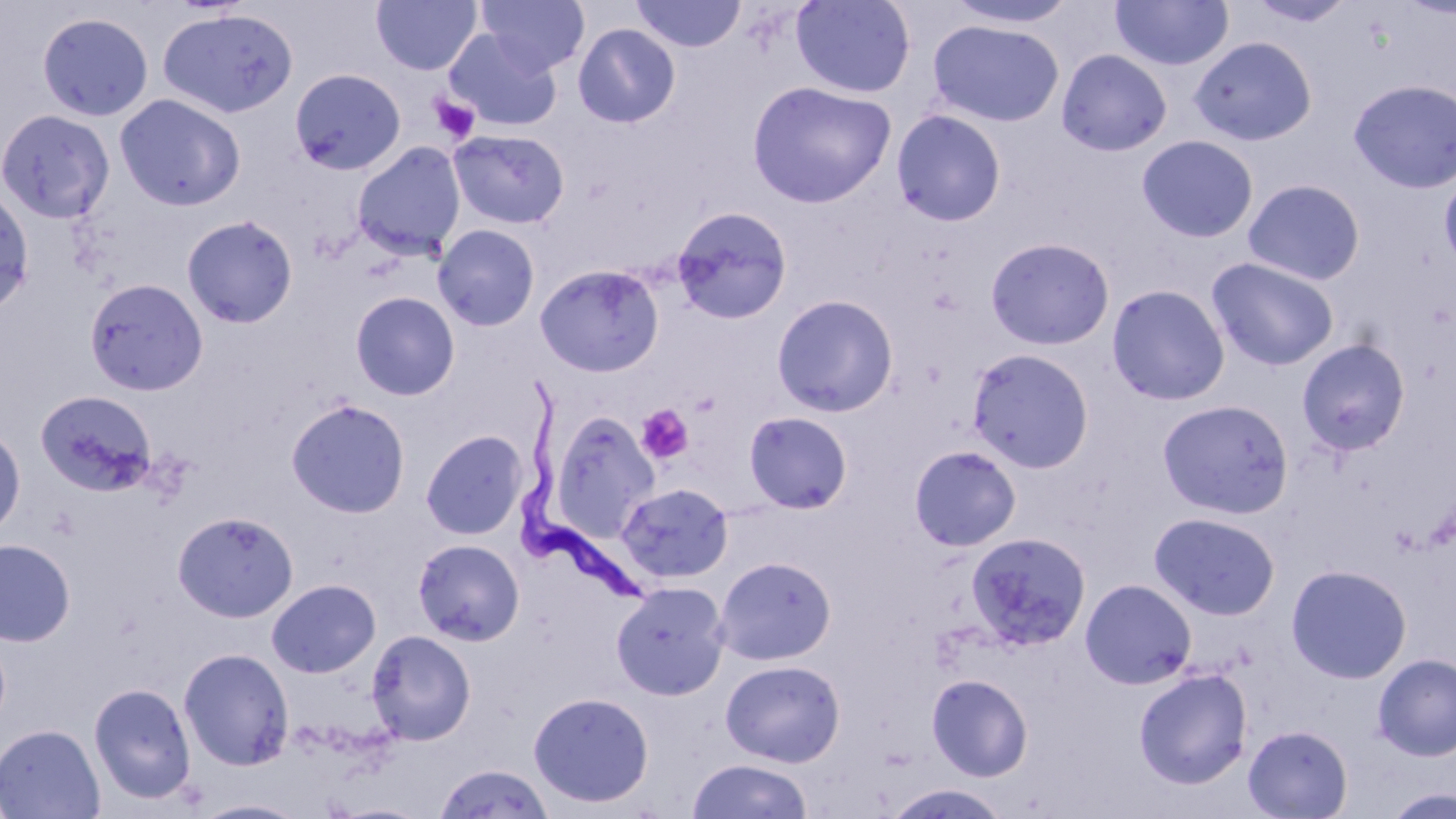
Trypanosoma brucei locations = approximate bounding boxes as (x1, y1, x2, y2) in pixels: (515, 377, 661, 608)
slide-level diagnosis = Trypanosoma brucei
magnification = 1000x
preparation = thin blood smear
stain = May-Grünwald-Giemsa
uninfected red blood cell locations = approximate bounding boxes as (x1, y1, x2, y2) in pixels: (371, 0, 481, 75), (476, 0, 589, 76), (630, 0, 746, 52), (790, 0, 916, 98), (941, 0, 1079, 30), (1110, 0, 1234, 72), (1245, 1, 1357, 28), (157, 8, 299, 119), (36, 11, 154, 122), (928, 20, 1065, 127), (573, 23, 681, 128), (444, 29, 562, 132), (1188, 36, 1318, 146), (1057, 49, 1173, 156), (290, 68, 406, 175), (1348, 79, 1456, 193), (746, 80, 897, 209), (115, 93, 246, 211), (1, 108, 115, 224), (891, 109, 1007, 226), (448, 129, 570, 229), (1137, 134, 1259, 242), (351, 142, 466, 260), (1439, 168, 1456, 277), (1243, 178, 1366, 285), (0, 185, 35, 317), (671, 205, 792, 324), (181, 214, 298, 329), (433, 224, 541, 331), (985, 237, 1115, 350), (1207, 257, 1340, 372), (535, 263, 664, 377), (85, 278, 209, 396), (1106, 284, 1230, 406), (350, 290, 460, 401), (772, 294, 899, 416), (1297, 338, 1411, 455), (966, 348, 1095, 473), (35, 389, 157, 495), (285, 398, 411, 518), (1157, 399, 1294, 519), (551, 411, 660, 536), (744, 411, 853, 514), (0, 425, 26, 539), (420, 430, 528, 540), (908, 445, 1022, 551), (617, 482, 734, 584), (172, 510, 298, 622), (1149, 512, 1280, 620), (965, 531, 1092, 652), (0, 538, 76, 647), (412, 538, 525, 646), (713, 556, 836, 665), (1286, 564, 1412, 684), (266, 578, 381, 678), (1081, 578, 1197, 689), (611, 581, 730, 700), (366, 629, 476, 745), (178, 647, 294, 771), (1373, 653, 1456, 761), (720, 659, 845, 767), (1133, 667, 1253, 789), (927, 673, 1033, 781), (89, 682, 197, 804), (528, 691, 654, 808), (0, 724, 105, 819), (1243, 724, 1352, 818), (687, 758, 813, 819), (433, 763, 556, 819), (883, 783, 1013, 818), (1382, 787, 1456, 819), (191, 797, 310, 818), (326, 802, 433, 819)
field of view = single
platelet locations = approximate bounding boxes as (x1, y1, x2, y2) in pixels: (430, 93, 480, 145), (637, 405, 694, 465)
image size = 1456×819 pixels
modality = optical microscopy